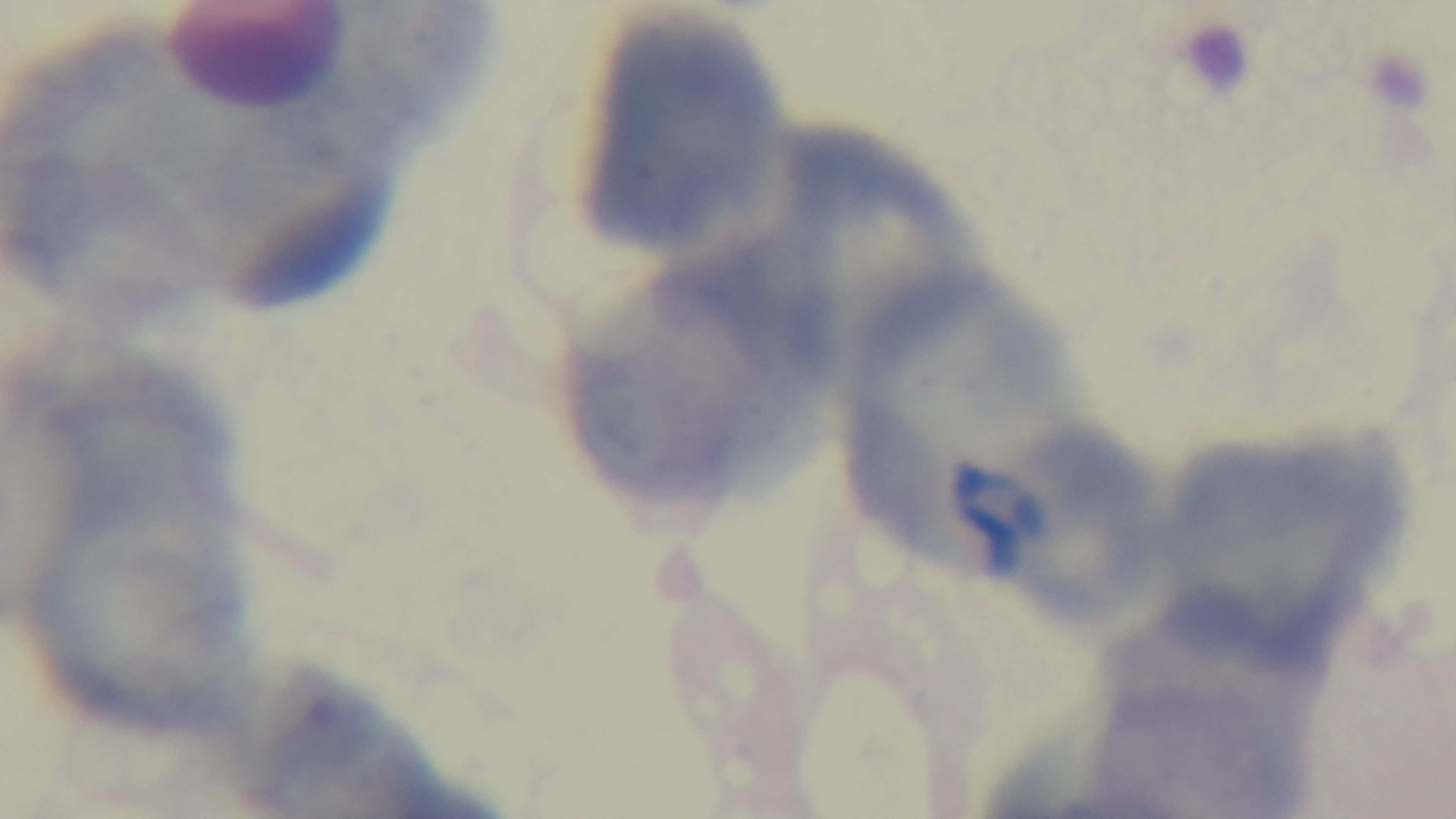 One field from the slide. Captured with a mounted 4K digital camera. Photomicrograph. Oil-immersion objective, 100x. Malaria status: uninfected. Giemsa stain. Preparation: thin smear.